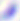

magnification = 400x
modality = micrograph
identification = Toxoplasma gondii